Identify the preparation type.
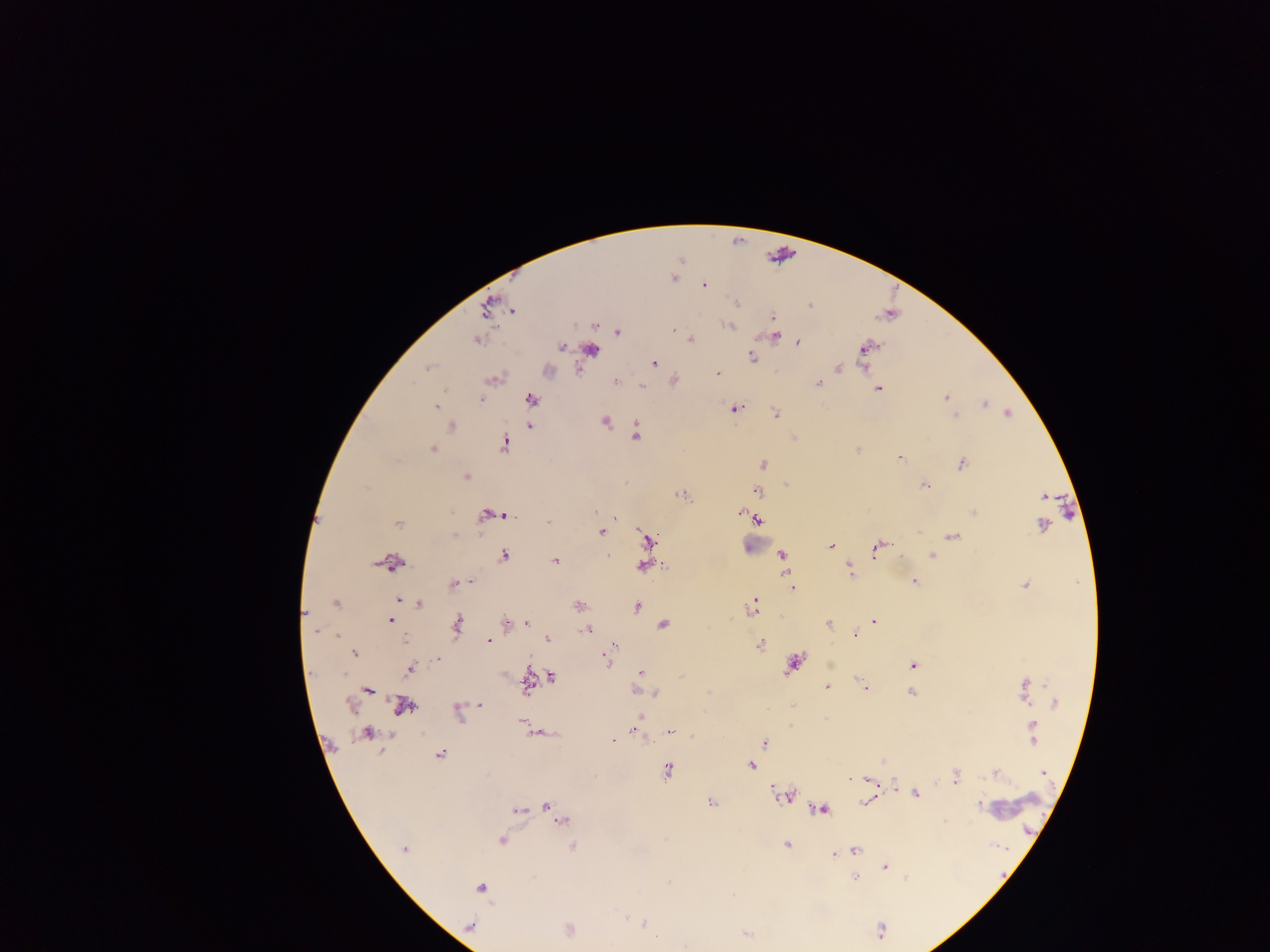
Thick blood smear.

capture = mobile-phone photograph through a microscope
country = Ghana
image size = 1270×952 pixels
malaria parasite locations = approximate centers as {x, y} in pixels: {674, 278}, {703, 285}, {735, 303}, {488, 306}, {810, 306}, {512, 311}, {772, 317}, {730, 325}, {594, 326}, {617, 331}, {773, 335}, {691, 339}, {477, 340}, {797, 342}, {561, 347}, {865, 348}, {590, 349}, {751, 356}, {654, 362}, {428, 367}, {838, 367}, {547, 370}, {716, 374}, {492, 379}, {615, 380}, {673, 381}, {818, 383}, {641, 385}, {878, 387}, {444, 391}, {946, 398}, {530, 399}, {481, 400}, {984, 403}, {436, 407}, {734, 408}, {775, 413}, {1008, 414}, {955, 415}, {605, 421}, {529, 425}, {450, 426}, {635, 434}, {794, 438}, {503, 443}, {857, 448}, {432, 449}, {898, 456}, {962, 462}, {763, 463}, {465, 477}, {924, 485}, {756, 491}, {682, 494}, {1043, 496}, {595, 510}, {739, 511}, {973, 511}, {502, 513}, {490, 514}, {756, 518}, {547, 521}, {397, 523}, {1043, 526}, {600, 531}, {950, 536}, {646, 540}, {830, 546}, {878, 547}, {503, 554}, {932, 554}, {781, 555}, {555, 560}, {390, 563}, {643, 566}, {848, 570}, {471, 581}, {914, 581}, {454, 584}, {1026, 584}, {792, 588}, {398, 599}, {336, 603}, {753, 603}, {419, 604}, {578, 605}, {636, 606}, {304, 613}, {391, 620}, {874, 620}, {505, 622}, {456, 623}, {528, 623}, {829, 623}, {663, 624}, {587, 629}, {315, 631}, {853, 634}, {547, 639}, {488, 641}, {759, 643}, {614, 644}, {611, 651}, {354, 653}, {604, 657}, {437, 659}, {793, 663}, {912, 665}, {410, 668}, {640, 673}, {552, 677}, {527, 683}, {828, 687}, {865, 688}, {367, 689}, {1025, 689}, {636, 690}, {910, 692}, {655, 693}, {1054, 703}, {479, 704}, {402, 706}, {457, 710}, {640, 717}, {522, 721}, {527, 726}, {1031, 726}, {636, 730}, {538, 732}, {671, 732}, {367, 733}, {1032, 734}, {613, 740}, {763, 742}, {439, 754}, {750, 765}, {667, 771}, {1043, 772}, {994, 773}, {955, 777}, {867, 779}, {893, 787}, {915, 794}, {788, 796}, {867, 801}, {709, 803}, {979, 803}, {545, 807}, {820, 808}, {517, 811}, {556, 815}, {561, 821}, {501, 840}, {786, 844}, {572, 845}, {404, 849}, {854, 849}, {835, 852}, {884, 867}, {854, 878}, {906, 878}, {669, 883}, {480, 888}, {645, 924}, {468, 926}, {568, 930}, {686, 945}
field of view = single